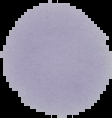

Summary:
  - Image size: 112×118 pixels
  - Preparation: thin blood smear
  - Image type: cell region segmented out of the field of view; surrounding area masked to black
  - Result: no malaria parasites seen